Outline each Plasmodium vivax-infected red blood cell.
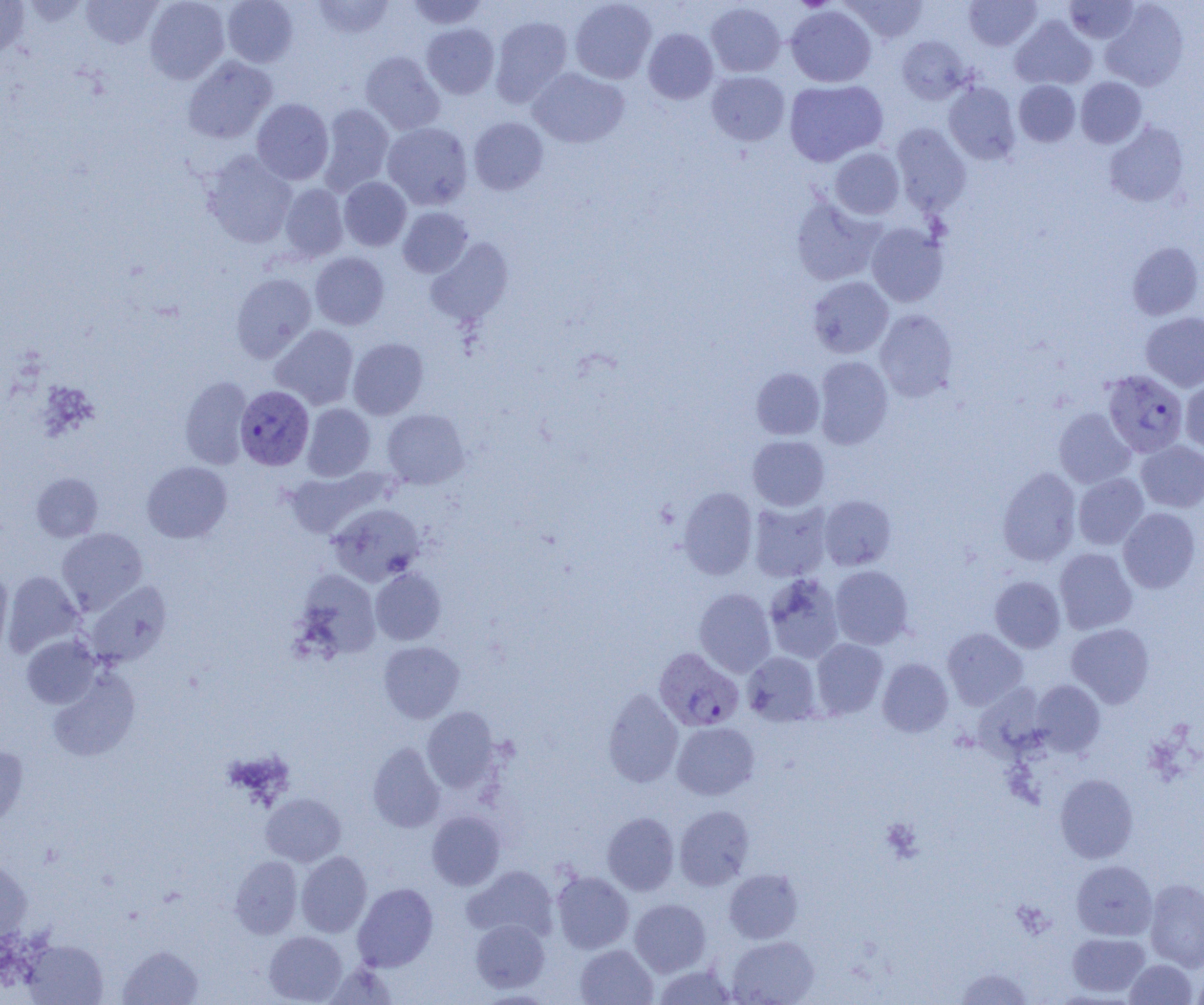
Approximate bounding boxes as named x1/y1/x2/y2 corners in pixels.
Plasmodium vivax-infected red blood cells: (x1=1102, y1=370, x2=1188, y2=457), (x1=235, y1=386, x2=314, y2=470), (x1=651, y1=645, x2=741, y2=729).

Summary:
  - Platelet locations: (x1=793, y1=0, x2=835, y2=12), (x1=880, y1=817, x2=923, y2=863)
  - Uninfected red blood cell locations: (x1=0, y1=0, x2=30, y2=57), (x1=80, y1=0, x2=162, y2=48), (x1=144, y1=0, x2=230, y2=83), (x1=222, y1=0, x2=298, y2=67), (x1=312, y1=0, x2=395, y2=39), (x1=405, y1=0, x2=490, y2=30), (x1=569, y1=0, x2=656, y2=84), (x1=842, y1=0, x2=928, y2=42), (x1=964, y1=0, x2=1041, y2=50), (x1=1063, y1=0, x2=1141, y2=44), (x1=1100, y1=1, x2=1190, y2=91), (x1=705, y1=2, x2=786, y2=77), (x1=786, y1=6, x2=876, y2=87), (x1=490, y1=16, x2=573, y2=106), (x1=1010, y1=16, x2=1097, y2=90), (x1=422, y1=23, x2=499, y2=98), (x1=643, y1=28, x2=718, y2=103), (x1=897, y1=35, x2=970, y2=104), (x1=360, y1=51, x2=445, y2=134), (x1=182, y1=56, x2=277, y2=144), (x1=528, y1=67, x2=629, y2=148), (x1=706, y1=71, x2=789, y2=145), (x1=1075, y1=77, x2=1147, y2=148), (x1=784, y1=79, x2=888, y2=166), (x1=1014, y1=80, x2=1080, y2=146), (x1=943, y1=81, x2=1020, y2=165), (x1=251, y1=99, x2=334, y2=185), (x1=318, y1=104, x2=394, y2=194), (x1=469, y1=117, x2=548, y2=194), (x1=1104, y1=121, x2=1190, y2=207), (x1=382, y1=123, x2=472, y2=210), (x1=891, y1=123, x2=971, y2=215), (x1=830, y1=148, x2=905, y2=219), (x1=202, y1=151, x2=297, y2=248), (x1=339, y1=177, x2=411, y2=251), (x1=279, y1=183, x2=349, y2=261), (x1=790, y1=196, x2=884, y2=286), (x1=397, y1=207, x2=473, y2=278), (x1=866, y1=222, x2=949, y2=307), (x1=425, y1=237, x2=514, y2=327), (x1=1127, y1=241, x2=1203, y2=320), (x1=310, y1=252, x2=389, y2=330), (x1=231, y1=272, x2=316, y2=362), (x1=808, y1=276, x2=894, y2=358), (x1=875, y1=309, x2=958, y2=402), (x1=1141, y1=312, x2=1204, y2=392), (x1=270, y1=324, x2=359, y2=409), (x1=348, y1=337, x2=428, y2=419), (x1=813, y1=356, x2=893, y2=449), (x1=751, y1=367, x2=825, y2=440), (x1=179, y1=376, x2=252, y2=469), (x1=1180, y1=376, x2=1204, y2=455), (x1=302, y1=403, x2=375, y2=481), (x1=382, y1=408, x2=469, y2=489), (x1=1054, y1=408, x2=1135, y2=488), (x1=747, y1=435, x2=829, y2=511), (x1=1136, y1=440, x2=1204, y2=512), (x1=142, y1=461, x2=232, y2=543), (x1=282, y1=467, x2=386, y2=539), (x1=997, y1=467, x2=1081, y2=566), (x1=31, y1=472, x2=103, y2=542), (x1=1073, y1=473, x2=1148, y2=550), (x1=678, y1=487, x2=758, y2=579), (x1=819, y1=495, x2=896, y2=570), (x1=748, y1=499, x2=833, y2=582), (x1=328, y1=503, x2=425, y2=586), (x1=1118, y1=508, x2=1200, y2=593), (x1=56, y1=527, x2=148, y2=614), (x1=1054, y1=547, x2=1137, y2=634), (x1=830, y1=565, x2=913, y2=649), (x1=370, y1=568, x2=446, y2=645), (x1=0, y1=569, x2=13, y2=657), (x1=295, y1=569, x2=382, y2=659), (x1=3, y1=570, x2=84, y2=656), (x1=763, y1=573, x2=845, y2=664), (x1=989, y1=576, x2=1065, y2=653), (x1=85, y1=581, x2=172, y2=666), (x1=694, y1=588, x2=776, y2=677), (x1=1066, y1=623, x2=1154, y2=707), (x1=942, y1=628, x2=1027, y2=710), (x1=21, y1=635, x2=101, y2=708), (x1=811, y1=638, x2=888, y2=719), (x1=379, y1=640, x2=464, y2=723), (x1=742, y1=651, x2=821, y2=725), (x1=877, y1=658, x2=953, y2=737), (x1=47, y1=668, x2=140, y2=762), (x1=1031, y1=680, x2=1105, y2=756), (x1=602, y1=688, x2=683, y2=787), (x1=422, y1=707, x2=501, y2=792), (x1=672, y1=721, x2=759, y2=800), (x1=367, y1=742, x2=445, y2=832), (x1=0, y1=745, x2=29, y2=828), (x1=1054, y1=773, x2=1138, y2=863), (x1=261, y1=792, x2=346, y2=867), (x1=675, y1=805, x2=755, y2=890), (x1=427, y1=811, x2=505, y2=890), (x1=602, y1=812, x2=680, y2=895), (x1=296, y1=851, x2=372, y2=937), (x1=230, y1=855, x2=303, y2=938), (x1=1071, y1=859, x2=1157, y2=940), (x1=0, y1=860, x2=33, y2=943), (x1=463, y1=865, x2=559, y2=942), (x1=724, y1=869, x2=803, y2=943), (x1=552, y1=871, x2=634, y2=953), (x1=1144, y1=878, x2=1204, y2=971), (x1=353, y1=882, x2=438, y2=971), (x1=630, y1=899, x2=711, y2=976), (x1=470, y1=919, x2=550, y2=993), (x1=264, y1=931, x2=347, y2=1004), (x1=1067, y1=932, x2=1150, y2=997), (x1=728, y1=935, x2=818, y2=1005), (x1=23, y1=940, x2=107, y2=1004), (x1=575, y1=944, x2=658, y2=1004), (x1=118, y1=945, x2=204, y2=1004), (x1=1125, y1=959, x2=1197, y2=1004), (x1=324, y1=962, x2=398, y2=1005), (x1=653, y1=963, x2=737, y2=1004), (x1=1191, y1=965, x2=1204, y2=1005), (x1=955, y1=967, x2=1032, y2=1004)
  - Slide-level diagnosis: Plasmodium vivax
  - Image size: 1204×1005 pixels
  - Field of view: one of a larger specimen
  - Modality: light microscopy
  - Magnification: 1000x
  - Preparation: thin blood smear